Classify this cell by malaria status.
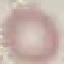

Uninfected.

capture = smartphone camera at the microscope eyepiece
stain = Giemsa
preparation = thin smear
image type = cell patch, automatically extracted from a larger field of view and resized to 64 × 64 pixels